Locate every blood parasite and identify its species.
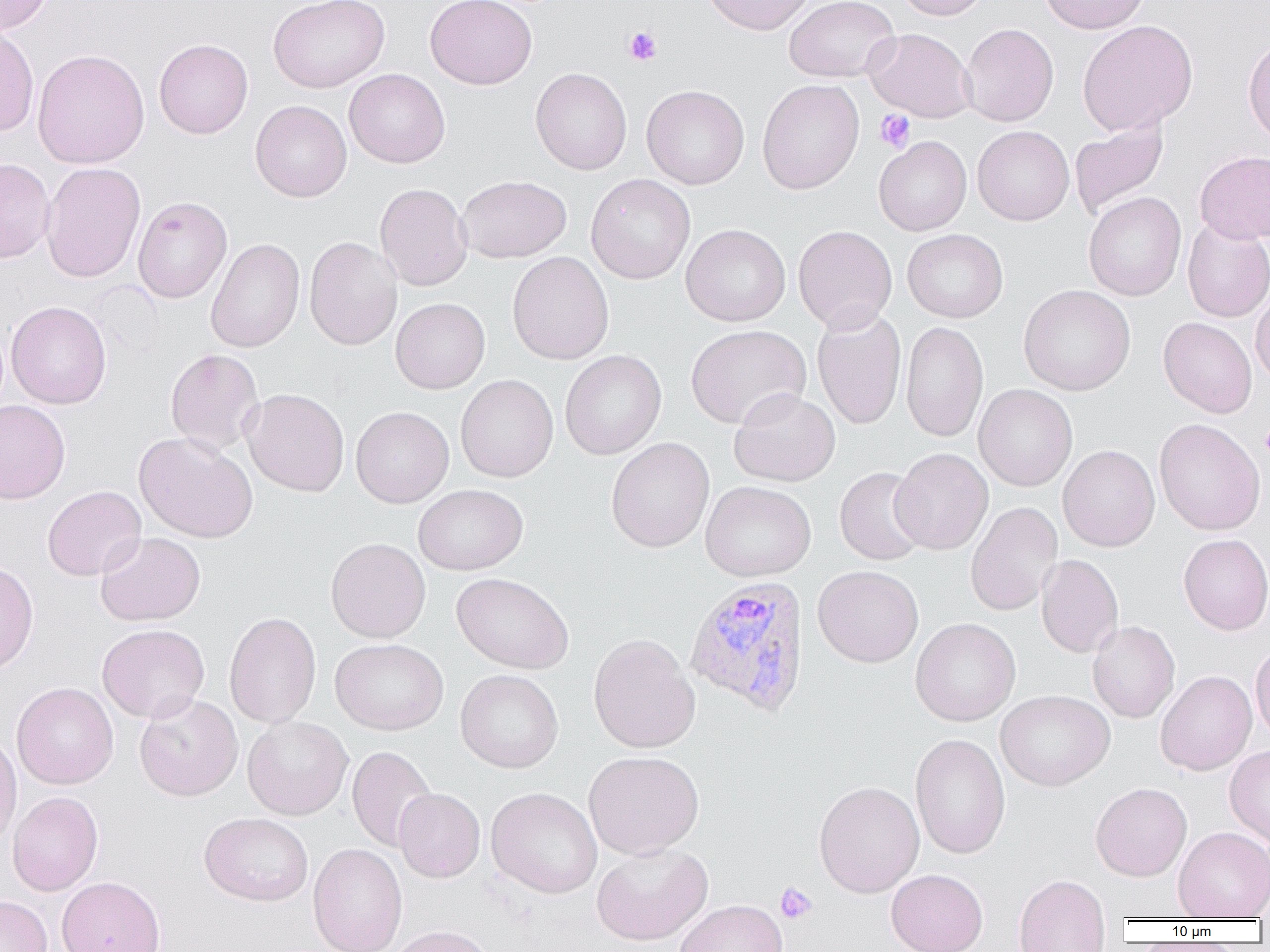
Approximate bounding boxes as [x1, y1, x2, y2] in pixels.
Plasmodium vivax-infected red blood cells: [684, 576, 810, 715].
No Plasmodium falciparum, Plasmodium ovale, Plasmodium malariae, Babesia divergens, or Trypanosoma brucei observed.

slide-level diagnosis = Plasmodium vivax
uninfected red blood cell locations = approximate bounding boxes as [x1, y1, x2, y2] in pixels: [0, 0, 53, 34], [268, 0, 389, 92], [426, 0, 537, 89], [703, 0, 816, 35], [784, 0, 900, 83], [894, 0, 991, 20], [1039, 0, 1150, 34], [1077, 20, 1198, 136], [960, 23, 1058, 127], [0, 24, 39, 137], [864, 28, 975, 122], [1243, 37, 1270, 145], [153, 39, 253, 139], [32, 49, 149, 169], [530, 67, 632, 175], [344, 68, 450, 168], [757, 79, 864, 194], [641, 85, 749, 189], [250, 100, 352, 202], [1070, 118, 1169, 219], [972, 126, 1074, 225], [874, 136, 971, 236], [1194, 150, 1270, 244], [0, 158, 55, 263], [40, 162, 146, 283], [585, 173, 695, 284], [457, 175, 571, 263], [374, 183, 472, 291], [1084, 192, 1186, 301], [132, 196, 232, 303], [1182, 219, 1270, 322], [680, 224, 790, 326], [793, 225, 897, 332], [902, 229, 1008, 323], [304, 237, 403, 350], [205, 238, 305, 353], [507, 252, 614, 365], [1019, 285, 1135, 395], [1251, 290, 1270, 386], [391, 298, 490, 394], [6, 301, 111, 409], [812, 306, 907, 430], [1158, 317, 1257, 418], [900, 321, 988, 442], [686, 324, 811, 429], [165, 348, 265, 455], [560, 350, 666, 460], [456, 374, 558, 482], [973, 384, 1077, 491], [242, 388, 349, 497], [729, 388, 840, 487], [0, 400, 70, 504], [351, 406, 454, 508], [1154, 418, 1265, 536], [133, 432, 258, 543], [606, 438, 714, 552], [1058, 444, 1160, 552], [890, 448, 993, 554], [834, 466, 929, 566], [700, 481, 816, 581], [413, 484, 528, 575], [42, 486, 146, 581], [966, 502, 1063, 616], [95, 532, 205, 626], [1179, 534, 1270, 635], [326, 538, 431, 642], [1036, 554, 1123, 658], [0, 561, 38, 676], [813, 565, 923, 667], [451, 572, 573, 674], [224, 611, 321, 729], [910, 618, 1020, 726], [1087, 620, 1180, 723], [97, 624, 210, 723], [588, 633, 700, 754], [330, 638, 448, 735], [1250, 642, 1270, 742], [456, 669, 564, 773], [1155, 670, 1257, 776], [12, 682, 118, 789], [995, 689, 1115, 791], [134, 693, 243, 801], [242, 716, 353, 820], [0, 733, 22, 849], [910, 733, 1010, 859], [1224, 745, 1270, 846], [347, 746, 437, 853], [583, 751, 704, 859], [814, 781, 924, 898], [1090, 782, 1192, 881], [486, 787, 603, 898], [394, 788, 485, 882], [7, 792, 103, 896], [199, 812, 314, 906], [1173, 826, 1270, 919], [308, 843, 407, 952], [591, 844, 713, 945], [886, 869, 988, 952], [1013, 874, 1110, 952], [56, 876, 166, 952], [0, 895, 52, 952], [674, 899, 788, 952], [388, 925, 496, 952]
image size = 1270×952 pixels
magnification = 1000x
field of view = single
preparation = thin blood film
platelet locations = approximate bounding boxes as [x1, y1, x2, y2] in pixels: [623, 26, 662, 65], [875, 109, 915, 152], [1259, 425, 1270, 456], [775, 882, 817, 924]
modality = light microscopy